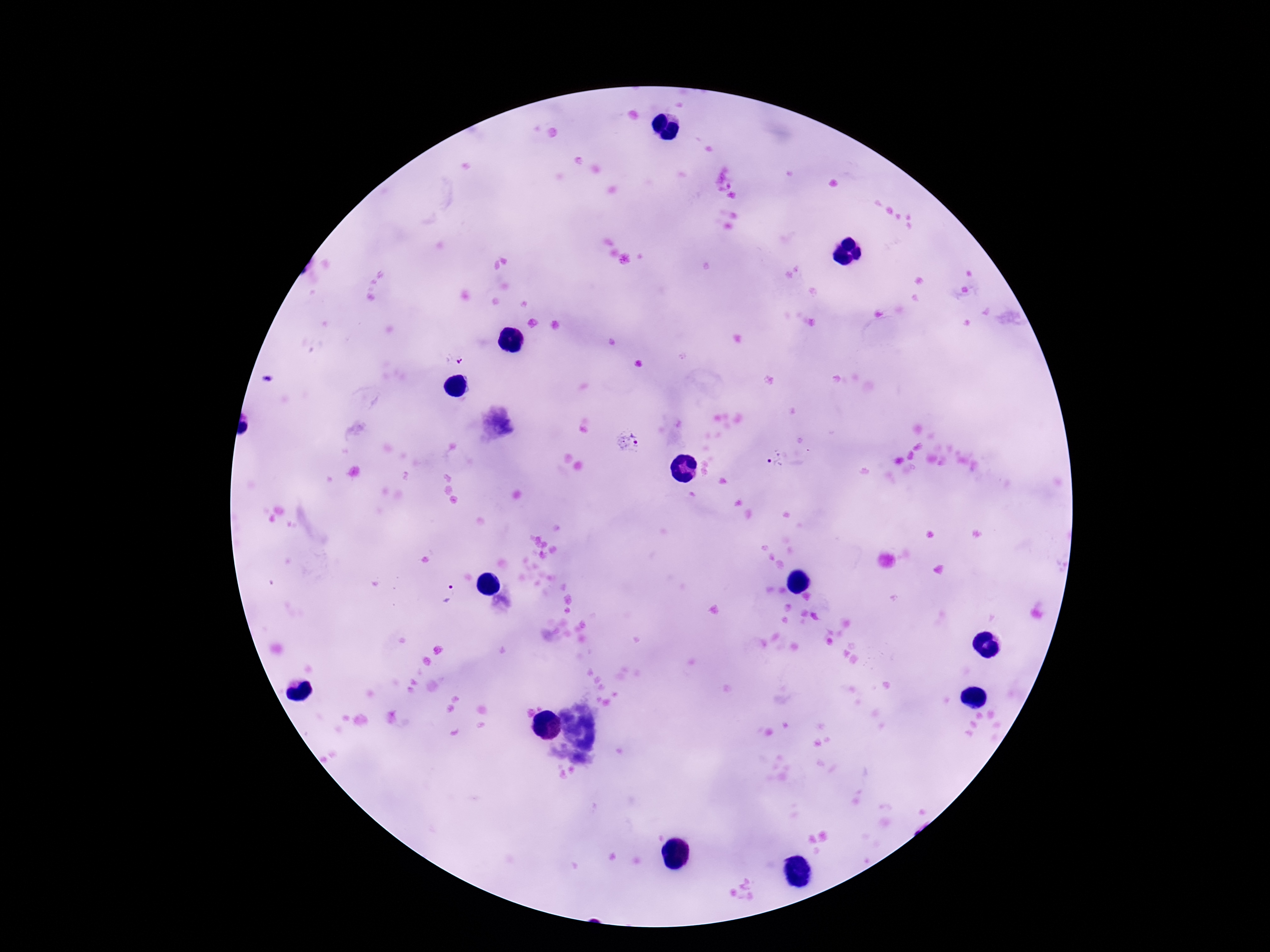
Plasmodium parasite locations = approximate centers as (x, y) in pixels: (454, 360), (629, 443), (777, 461), (450, 596)
patient malaria status = positive
magnification = 100x
capture = smartphone camera through the microscope eyepiece
field of view = single
preparation = thick peripheral-blood smear
stain = Giemsa
image size = 1270×952 pixels